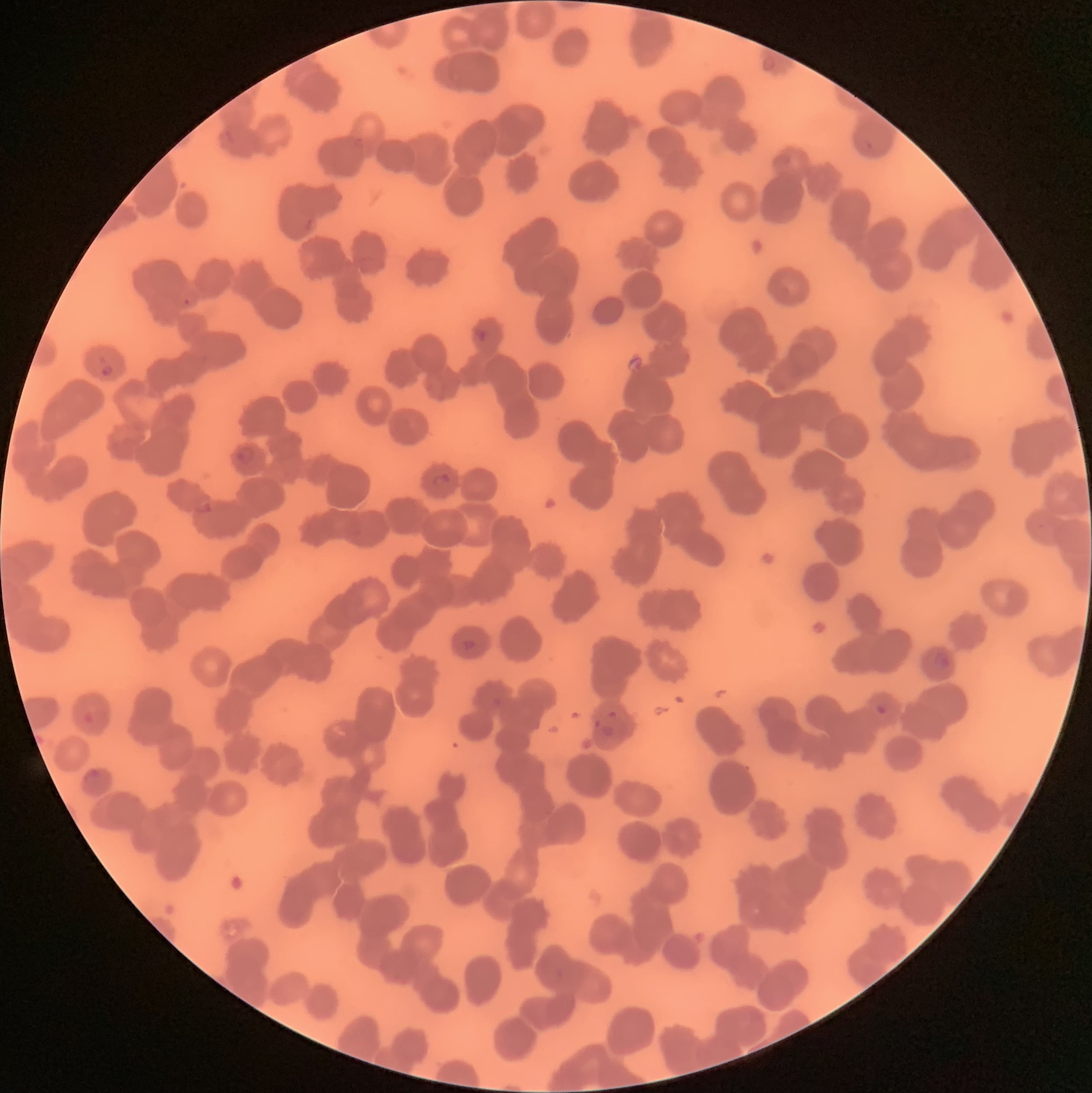
coordinate format = approximate bounding boxes as [x1, y1, x2, y2] in pixels
Plasmodium parasite locations = [183, 299, 191, 306], [476, 329, 488, 343], [100, 364, 114, 376], [236, 446, 255, 464], [432, 474, 452, 490], [195, 502, 212, 514], [462, 638, 477, 650], [933, 651, 950, 670], [875, 704, 887, 716], [82, 711, 93, 723], [82, 769, 103, 788]
modality = optical microscopy
red blood cell morphology = rouleaux formation
preparation = thin blood film
image size = 1092×1093 pixels